Report the malaria status of this cell.
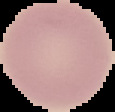
Uninfected.

Summary:
  - Preparation: thin blood smear
  - Image type: segmented cell region with the area outside set to black
  - Image size: 115×112 pixels